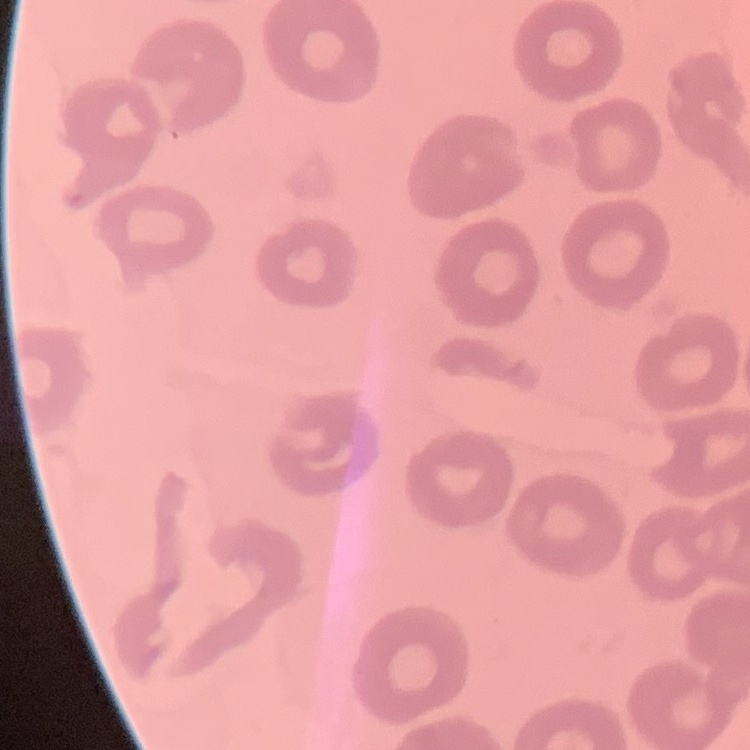
red blood cell morphology = no rouleaux formation
preparation = thin peripheral smear
image type = square crop of a larger photomicrograph
stain = Field's or Giemsa